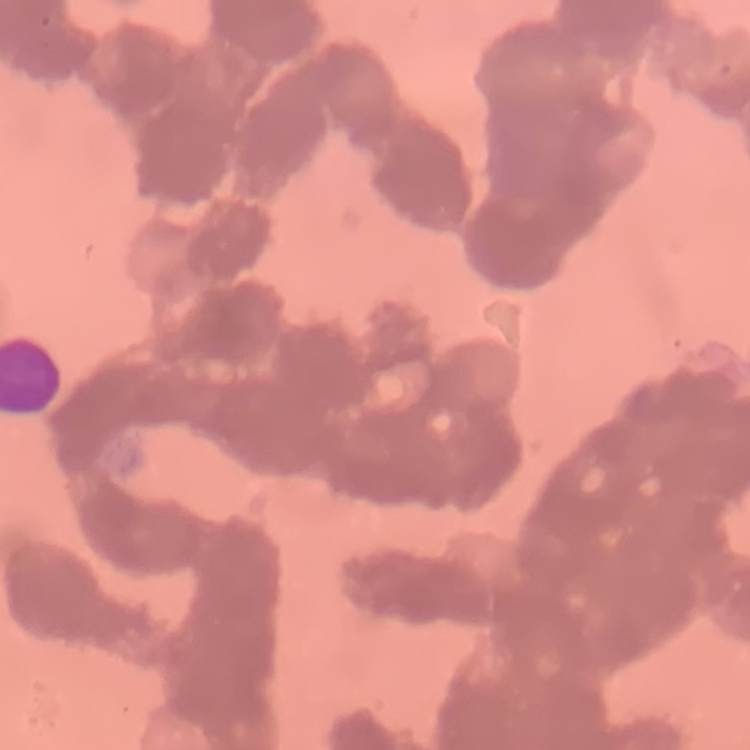
Summary:
  - Erythrocyte morphology: rouleaux formation
  - Image type: one tile cut from a larger photomicrograph
  - Stain: Field's or Giemsa
  - Preparation: thin blood film